Assess this cell for malaria.
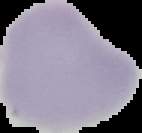

It is uninfected.

From a thin blood smear. The area outside the segmented cell region is set to black. Image is 142×133 pixels.